Classify this cell by malaria status.
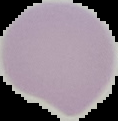
Uninfected.

Summary:
  - Preparation: thin blood smear
  - Image size: 118×121 pixels
  - Image type: segmented cell region with the area outside set to black